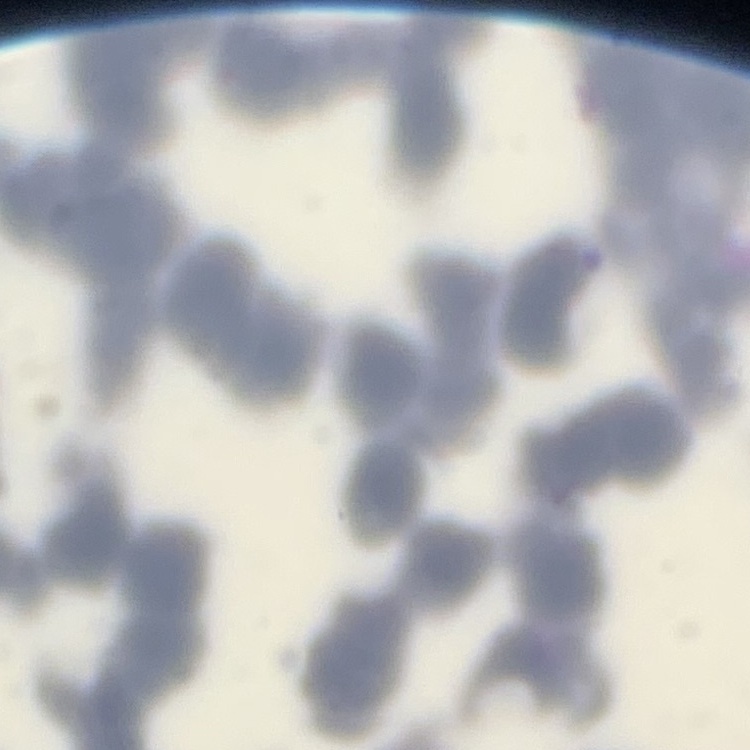

erythrocyte morphology = rouleaux formation
preparation = thin blood film
stain = Field's or Giemsa
image type = square crop of a larger photomicrograph